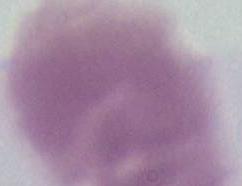

magnification = 1000x
modality = photomicrograph
identification = red blood cell